Classify this cell by malaria status.
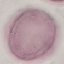
It is uninfected.

Photographed with a smartphone camera at the microscope eyepiece. Giemsa stain. Cell patch, automatically extracted from a larger field of view and resized to 64 × 64 pixels. Thin blood smear.